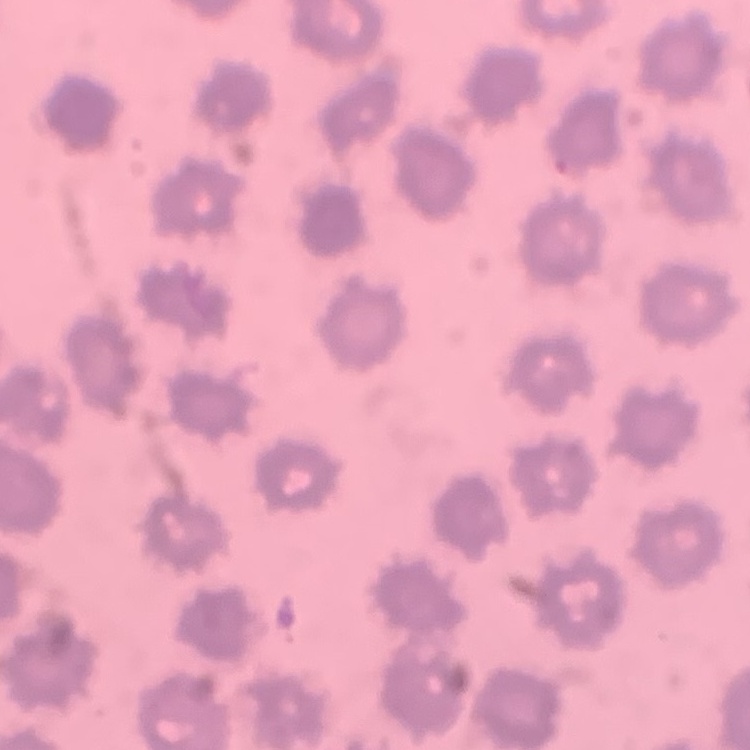
The erythrocytes exhibit no rouleaux formation. One tile cut from a larger photomicrograph. Field's or Giemsa stain. Thin blood film.